State which parasite is depicted.
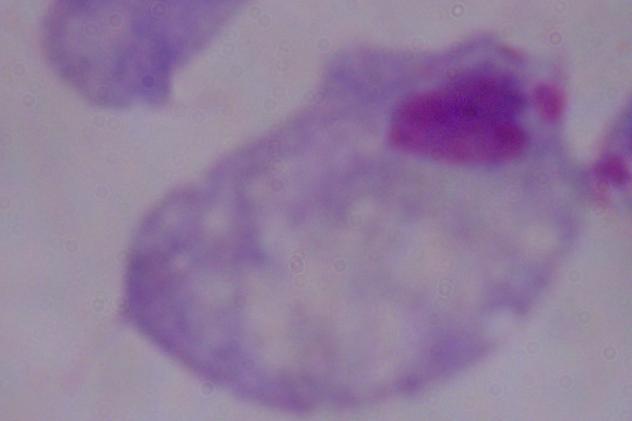

This is a trichomonad.

Summary:
  - Magnification: 1000x
  - Modality: photomicrograph